State which cell type is depicted.
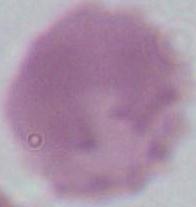
This is an erythrocyte.

Micrograph. 1000x magnification.